Give the extent of all Plasmodium vivax-infected red blood cells.
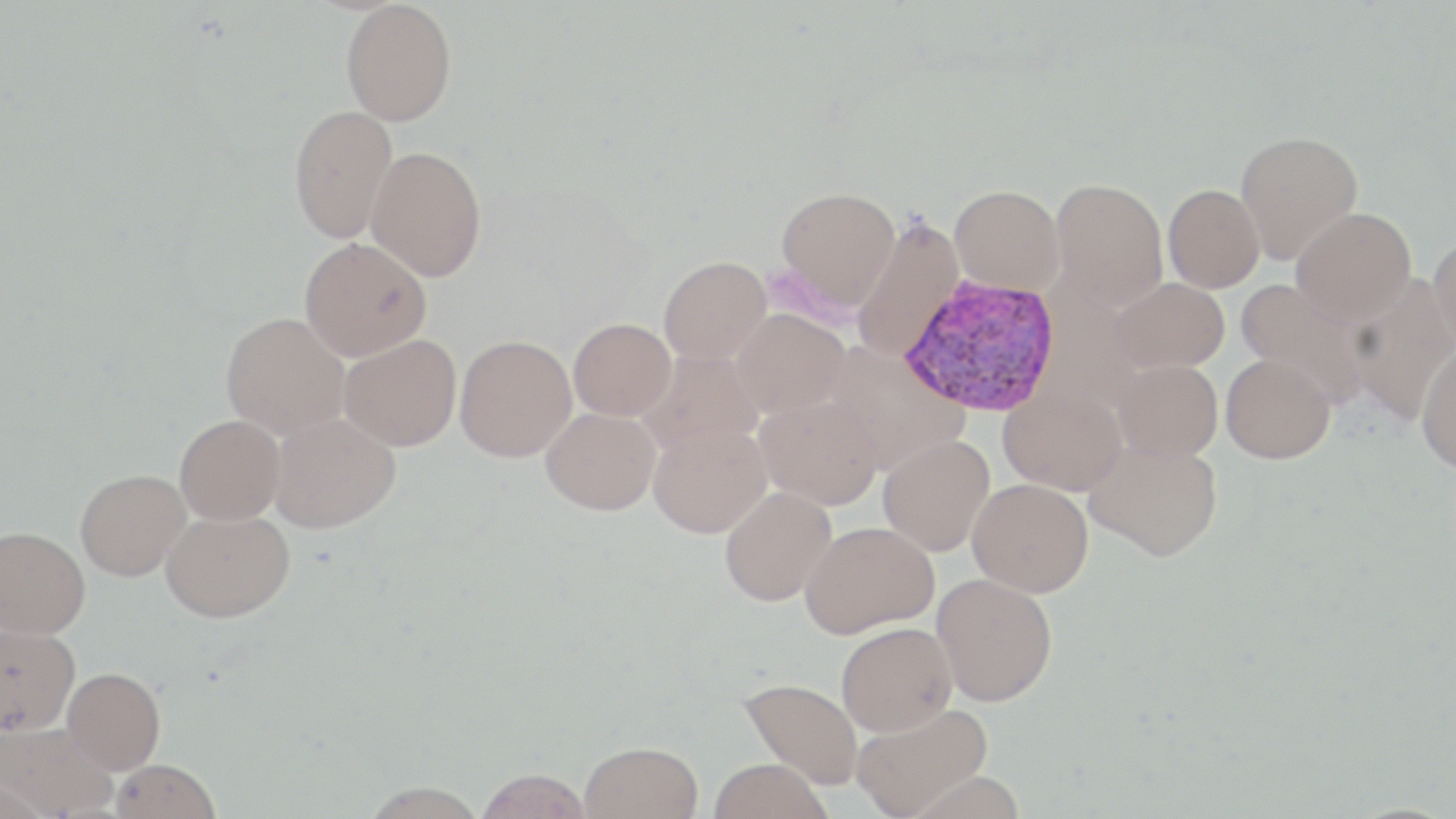

Approximate bounding boxes as named x1/y1/x2/y2 corners in pixels.
Plasmodium vivax-infected red blood cells: (x1=899, y1=275, x2=1062, y2=416).

Summary:
  - Uninfected red blood cell locations: (x1=341, y1=1, x2=457, y2=126), (x1=289, y1=104, x2=398, y2=244), (x1=1234, y1=130, x2=1364, y2=264), (x1=365, y1=146, x2=487, y2=281), (x1=1049, y1=177, x2=1169, y2=312), (x1=950, y1=184, x2=1064, y2=295), (x1=1163, y1=184, x2=1265, y2=292), (x1=776, y1=186, x2=901, y2=312), (x1=1291, y1=208, x2=1416, y2=325), (x1=852, y1=215, x2=965, y2=362), (x1=1429, y1=232, x2=1456, y2=360), (x1=299, y1=238, x2=432, y2=360), (x1=659, y1=255, x2=771, y2=365), (x1=1344, y1=274, x2=1456, y2=425), (x1=1108, y1=278, x2=1230, y2=373), (x1=1235, y1=278, x2=1370, y2=406), (x1=731, y1=309, x2=849, y2=417), (x1=221, y1=312, x2=350, y2=440), (x1=569, y1=318, x2=676, y2=420), (x1=339, y1=333, x2=462, y2=451), (x1=455, y1=335, x2=577, y2=462), (x1=824, y1=343, x2=969, y2=471), (x1=1416, y1=345, x2=1456, y2=473), (x1=638, y1=349, x2=765, y2=455), (x1=1222, y1=354, x2=1336, y2=463), (x1=1112, y1=359, x2=1222, y2=462), (x1=999, y1=385, x2=1127, y2=495), (x1=755, y1=394, x2=882, y2=510), (x1=541, y1=407, x2=660, y2=515), (x1=269, y1=412, x2=400, y2=534), (x1=175, y1=415, x2=285, y2=524), (x1=648, y1=423, x2=771, y2=538), (x1=878, y1=434, x2=995, y2=556), (x1=1084, y1=436, x2=1223, y2=560), (x1=76, y1=469, x2=190, y2=580), (x1=967, y1=478, x2=1093, y2=597), (x1=719, y1=486, x2=837, y2=606), (x1=161, y1=508, x2=294, y2=622), (x1=800, y1=522, x2=939, y2=637), (x1=0, y1=526, x2=90, y2=638), (x1=933, y1=574, x2=1058, y2=706), (x1=836, y1=622, x2=957, y2=736), (x1=1, y1=623, x2=80, y2=736), (x1=62, y1=668, x2=165, y2=774), (x1=740, y1=677, x2=864, y2=789), (x1=851, y1=702, x2=993, y2=818), (x1=0, y1=722, x2=118, y2=818), (x1=579, y1=741, x2=704, y2=819), (x1=708, y1=758, x2=832, y2=819), (x1=110, y1=759, x2=221, y2=819), (x1=475, y1=768, x2=592, y2=819), (x1=0, y1=778, x2=47, y2=819), (x1=360, y1=780, x2=487, y2=819)
  - Slide-level diagnosis: Plasmodium vivax
  - Field of view: single
  - Preparation: thin blood smear
  - Stain: May-Grünwald-Giemsa
  - Magnification: 1000x
  - Modality: optical microscopy
  - Image size: 1456×819 pixels